Assess this cell for malaria.
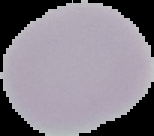
Uninfected.

Summary:
  - Image size: 154×136 pixels
  - Image type: segmented cell region on a black background
  - Preparation: thin blood film